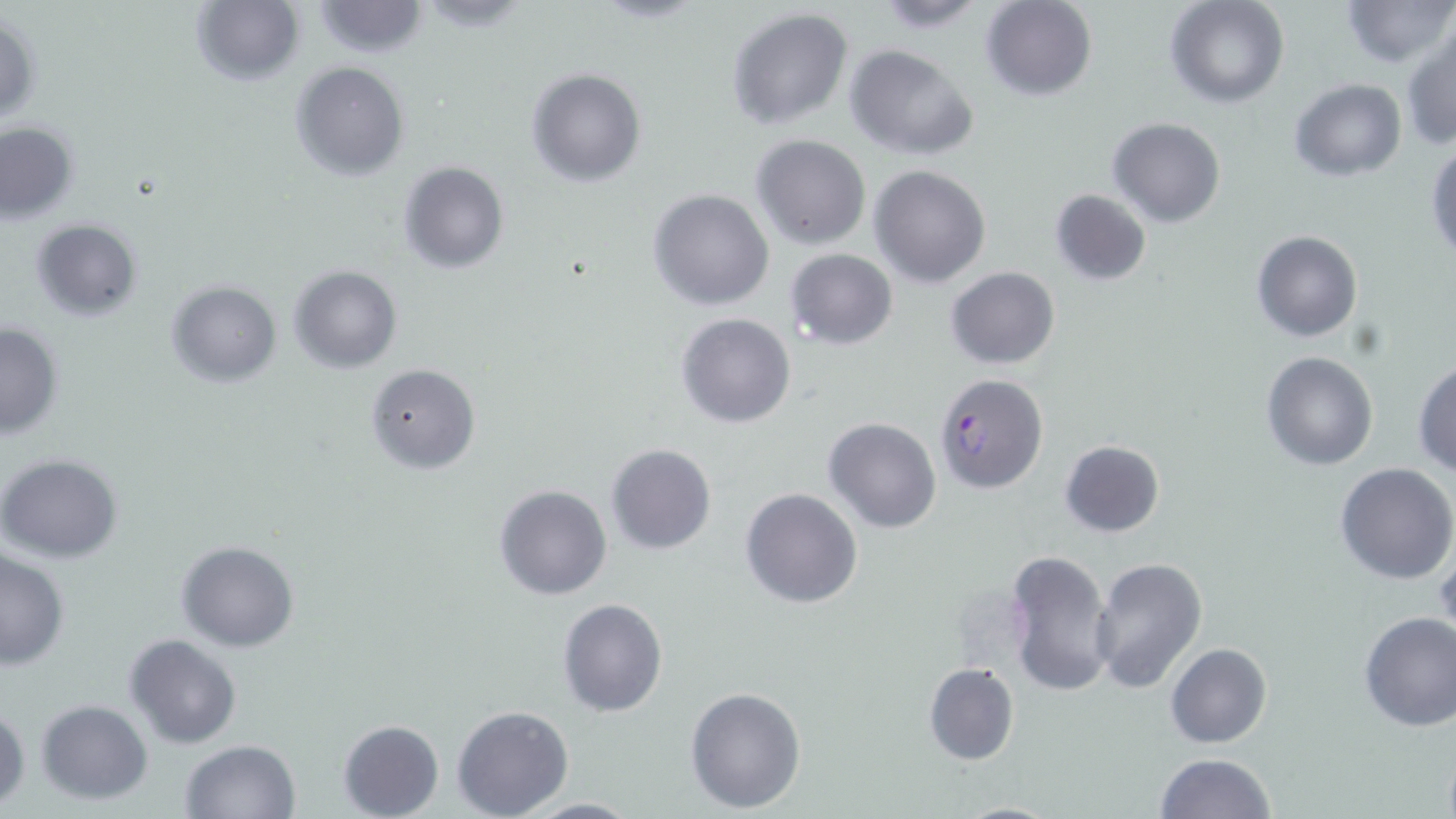

Summary:
  - Coordinate format: approximate bounding boxes as (x1, y1, x2, y2) in pixels
  - Plasmodium falciparum-infected red blood cell locations: (933, 373, 1047, 493)
  - Uninfected red blood cell locations: (190, 0, 304, 87), (869, 0, 994, 31), (980, 0, 1099, 101), (1165, 0, 1291, 108), (1341, 0, 1454, 68), (310, 1, 428, 57), (727, 9, 854, 130), (1, 13, 41, 126), (1402, 25, 1456, 151), (844, 44, 979, 161), (290, 61, 409, 181), (526, 68, 646, 187), (1289, 79, 1407, 182), (1107, 116, 1226, 227), (0, 121, 81, 225), (751, 135, 872, 250), (1427, 145, 1456, 263), (398, 162, 509, 274), (869, 164, 991, 288), (1049, 188, 1151, 286), (649, 189, 775, 311), (30, 218, 142, 321), (1251, 230, 1363, 343), (786, 248, 897, 349), (288, 265, 403, 373), (946, 266, 1059, 370), (166, 280, 283, 387), (677, 312, 797, 428), (0, 323, 64, 440), (1261, 352, 1379, 472), (1412, 360, 1456, 476), (364, 362, 481, 473), (824, 417, 941, 532), (1059, 440, 1164, 537), (606, 444, 715, 554), (0, 453, 124, 564), (1335, 463, 1456, 585), (495, 485, 612, 600), (739, 488, 863, 609), (177, 540, 301, 652), (0, 548, 71, 670), (1005, 548, 1115, 698), (1091, 557, 1207, 693), (556, 599, 668, 717), (1357, 611, 1456, 731), (125, 635, 242, 749), (1164, 643, 1273, 748), (923, 663, 1019, 766), (685, 685, 807, 814), (36, 699, 153, 804), (0, 704, 29, 810), (451, 705, 574, 819), (338, 719, 443, 819), (179, 740, 301, 819), (1155, 751, 1275, 819), (519, 796, 642, 817), (950, 800, 1066, 818)
  - Slide-level diagnosis: Plasmodium falciparum
  - Stain: May-Grünwald-Giemsa
  - Magnification: 1000x
  - Image size: 1456×819 pixels
  - Preparation: thin blood film
  - Modality: light microscopy
  - Field of view: single